Assess for Plasmodium parasites.
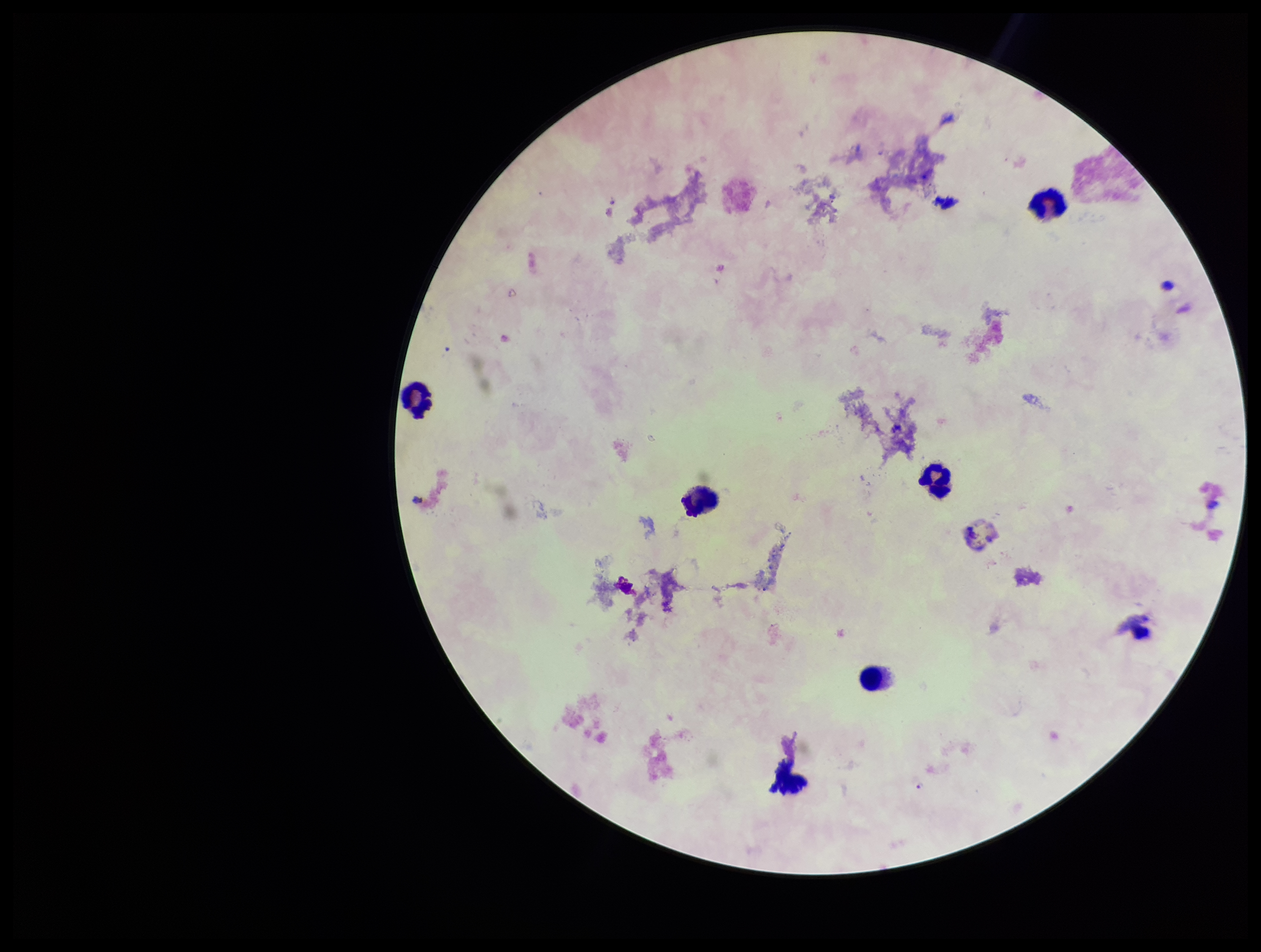

None detected.

Summary:
  - Preparation: thick
  - Field of view: single
  - Stain: Giemsa
  - Capture: smartphone photograph through the microscope eyepiece
  - Species reported for this patient: Plasmodium falciparum
  - Image size: 1261×952 pixels
  - Parasite count: 0
  - Patient malaria status: positive
  - Leukocyte count: 7